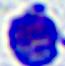 Photomicrograph. A leukocyte is shown. Captured at 400x magnification.